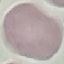
Summary:
  - Malaria status: uninfected
  - Preparation: thin blood smear
  - Stain: Giemsa
  - Image type: cell patch, automatically extracted from a larger field of view and resized to 64 × 64 pixels
  - Capture: smartphone camera at the microscope eyepiece